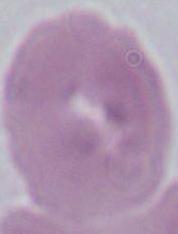
Summary:
  - Magnification: 1000x
  - Identification: erythrocyte
  - Modality: photomicrograph